Classify this cell by malaria status.
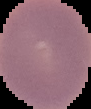

Uninfected.

Segmented cell region on a black background. Image is 91×109 pixels. From a thin blood film.